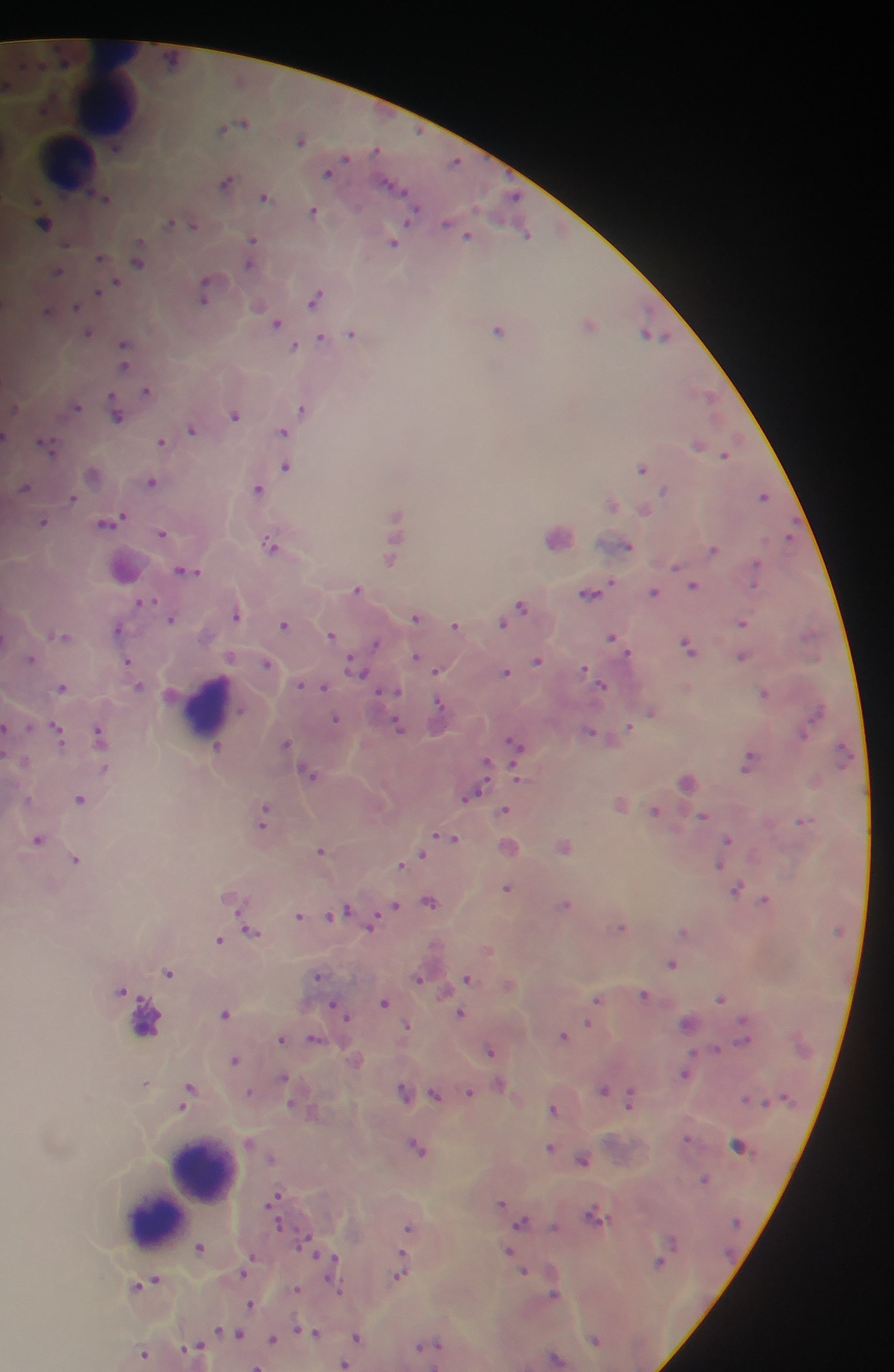
Approximate centers as {x, y} in pixels. Plasmodium parasite locations: {239, 121}, {302, 138}, {456, 162}, {329, 170}, {227, 180}, {266, 195}, {105, 197}, {314, 209}, {44, 219}, {181, 222}, {455, 226}, {464, 231}, {526, 233}, {252, 240}, {393, 240}, {101, 256}, {138, 257}, {251, 257}, {57, 271}, {109, 285}, {206, 289}, {101, 290}, {316, 295}, {50, 309}, {277, 320}, {590, 321}, {499, 328}, {88, 331}, {353, 332}, {652, 333}, {335, 336}, {322, 337}, {295, 345}, {126, 350}, {148, 390}, {708, 394}, {75, 404}, {304, 406}, {118, 408}, {235, 413}, {193, 427}, {284, 430}, {7, 435}, {163, 441}, {48, 443}, {699, 443}, {726, 452}, {288, 465}, {643, 466}, {93, 472}, {153, 480}, {24, 487}, {258, 487}, {765, 495}, {73, 496}, {612, 501}, {646, 508}, {398, 515}, {109, 520}, {45, 521}, {163, 532}, {559, 534}, {272, 542}, {626, 544}, {714, 547}, {391, 556}, {125, 566}, {677, 567}, {187, 568}, {695, 583}, {358, 588}, {589, 591}, {653, 591}, {144, 601}, {521, 606}, {237, 612}, {417, 615}, {171, 617}, {505, 619}, {743, 620}, {286, 623}, {456, 624}, {119, 627}, {333, 633}, {62, 635}, {614, 636}, {688, 644}, {742, 654}, {31, 656}, {418, 656}, {538, 659}, {129, 662}, {268, 662}, {357, 664}, {438, 669}, {506, 669}, {601, 683}, {303, 684}, {62, 685}, {322, 686}, {395, 689}, {766, 690}, {652, 711}, {439, 712}, {337, 718}, {399, 725}, {8, 730}, {59, 730}, {102, 734}, {516, 743}, {287, 744}, {218, 746}, {750, 759}, {487, 762}, {311, 771}, {519, 777}, {688, 780}, {473, 793}, {82, 797}, {621, 801}, {506, 809}, {656, 810}, {265, 814}, {703, 815}, {804, 818}, {447, 836}, {39, 838}, {728, 839}, {565, 844}, {509, 845}, {323, 849}, {415, 856}, {77, 857}, {406, 861}, {720, 864}, {509, 886}, {737, 887}, {234, 896}, {766, 898}, {430, 899}, {566, 903}, {394, 905}, {340, 912}, {300, 914}, {372, 921}, {622, 925}, {252, 929}, {685, 930}, {220, 939}, {489, 949}, {673, 962}, {170, 970}, {320, 973}, {419, 977}, {468, 977}, {510, 982}, {123, 988}, {126, 992}, {645, 993}, {721, 996}, {598, 999}, {386, 1001}, {339, 1006}, {226, 1012}, {461, 1012}, {689, 1021}, {590, 1023}, {408, 1024}, {564, 1034}, {282, 1037}, {315, 1038}, {716, 1047}, {491, 1048}, {356, 1058}, {236, 1059}, {686, 1073}, {284, 1077}, {146, 1082}, {500, 1083}, {604, 1089}, {405, 1090}, {189, 1091}, {469, 1091}, {250, 1092}, {436, 1093}, {631, 1098}, {554, 1107}, {250, 1142}, {738, 1144}, {419, 1145}, {552, 1146}, {583, 1157}, {273, 1158}, {704, 1178}, {275, 1198}, {503, 1202}, {596, 1214}, {521, 1221}, {410, 1227}, {201, 1246}, {509, 1250}, {331, 1258}, {659, 1261}, {526, 1269}, {246, 1270}, {400, 1271}, {146, 1283}, {298, 1290}, {554, 1294}, {251, 1303}, {221, 1331}, {310, 1331}, {240, 1334}, {358, 1336}, {273, 1338}, {596, 1339}, {431, 1344}, {196, 1346}, {145, 1352}, {556, 1357}, {344, 1363}, {257, 1366}. Object labeled both Plasmodium parasite and leukocyte by the source: {145, 1017}. Leukocyte locations: {106, 92}, {66, 160}, {209, 706}, {202, 1171}, {180, 1199}, {153, 1219}. Collected in Ghana. Single field of view. Photographed through a microscope with a mobile-phone camera. Thick blood smear. Image is 894×1372 pixels.